Comment on the morphology of the erythrocytes.
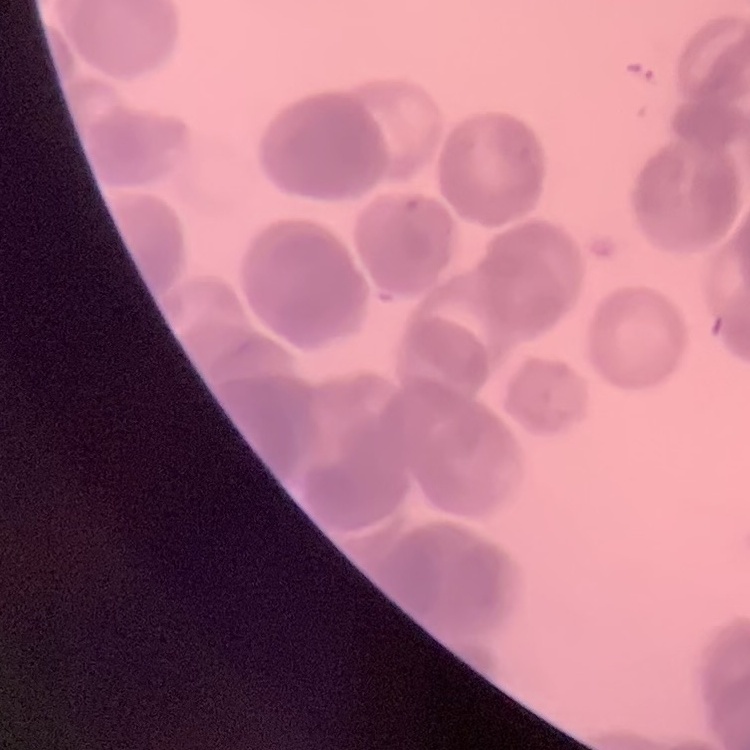

Rouleaux formation.

image type = one tile cut from a larger photomicrograph
stain = Field's or Giemsa
preparation = thin blood smear